Name the cell type shown.
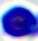

A leukocyte.

Captured at 400x magnification. Micrograph.